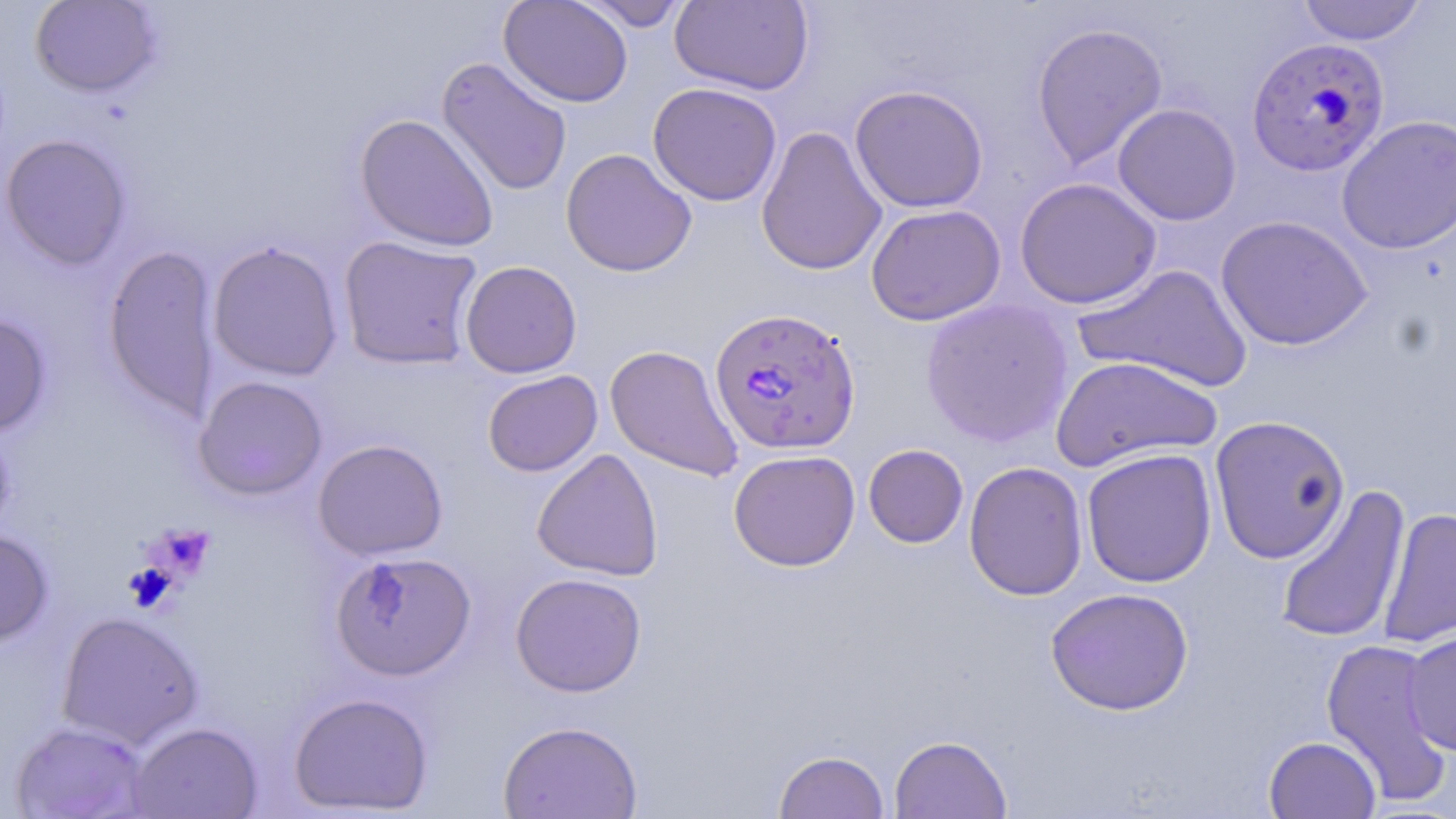

slide-level diagnosis = Plasmodium falciparum
uninfected red blood cell locations = approximate bounding boxes as (x1,y1)-(x2,y2) corner pairs in pixels: (29,0)-(162,98), (498,0)-(633,107), (670,0)-(814,96), (1296,0)-(1428,45), (576,1)-(693,31), (1031,22)-(1168,171), (436,56)-(573,197), (647,81)-(782,206), (849,84)-(989,212), (1112,104)-(1242,225), (355,113)-(499,252), (1335,115)-(1456,255), (756,125)-(887,276), (0,134)-(131,269), (560,147)-(697,277), (1014,177)-(1161,309), (866,204)-(1006,326), (1215,215)-(1373,351), (338,235)-(484,370), (207,241)-(343,381), (103,244)-(221,422), (460,260)-(582,378), (1074,263)-(1253,393), (920,298)-(1074,448), (0,314)-(52,437), (604,344)-(744,482), (1049,355)-(1221,473), (482,370)-(602,476), (193,375)-(328,500), (1209,415)-(1350,564), (313,438)-(448,560), (863,444)-(969,548), (532,448)-(663,581), (1081,448)-(1217,588), (728,449)-(861,571), (963,461)-(1088,601), (1274,483)-(1411,645), (1378,506)-(1456,650), (0,530)-(53,646), (331,550)-(476,681), (510,573)-(647,697), (1045,587)-(1194,715), (55,611)-(204,749), (1401,629)-(1456,757), (1319,638)-(1452,805), (288,692)-(433,815), (10,720)-(151,818), (498,720)-(643,818), (129,721)-(263,818), (889,734)-(1012,819), (1263,735)-(1381,819), (774,750)-(889,819)
stain = May-Grünwald-Giemsa
modality = optical microscopy
preparation = thin blood film
field of view = one of a larger specimen
platelet locations = approximate bounding boxes as (x1,y1)-(x2,y2) corner pairs in pixels: (145,522)-(215,583), (123,563)-(178,613)
Plasmodium falciparum-infected red blood cell locations = approximate bounding boxes as (x1,y1)-(x2,y2) corner pairs in pixels: (1245,37)-(1391,177), (709,305)-(861,455)
image size = 1456×819 pixels
magnification = 1000x